Outline platelets.
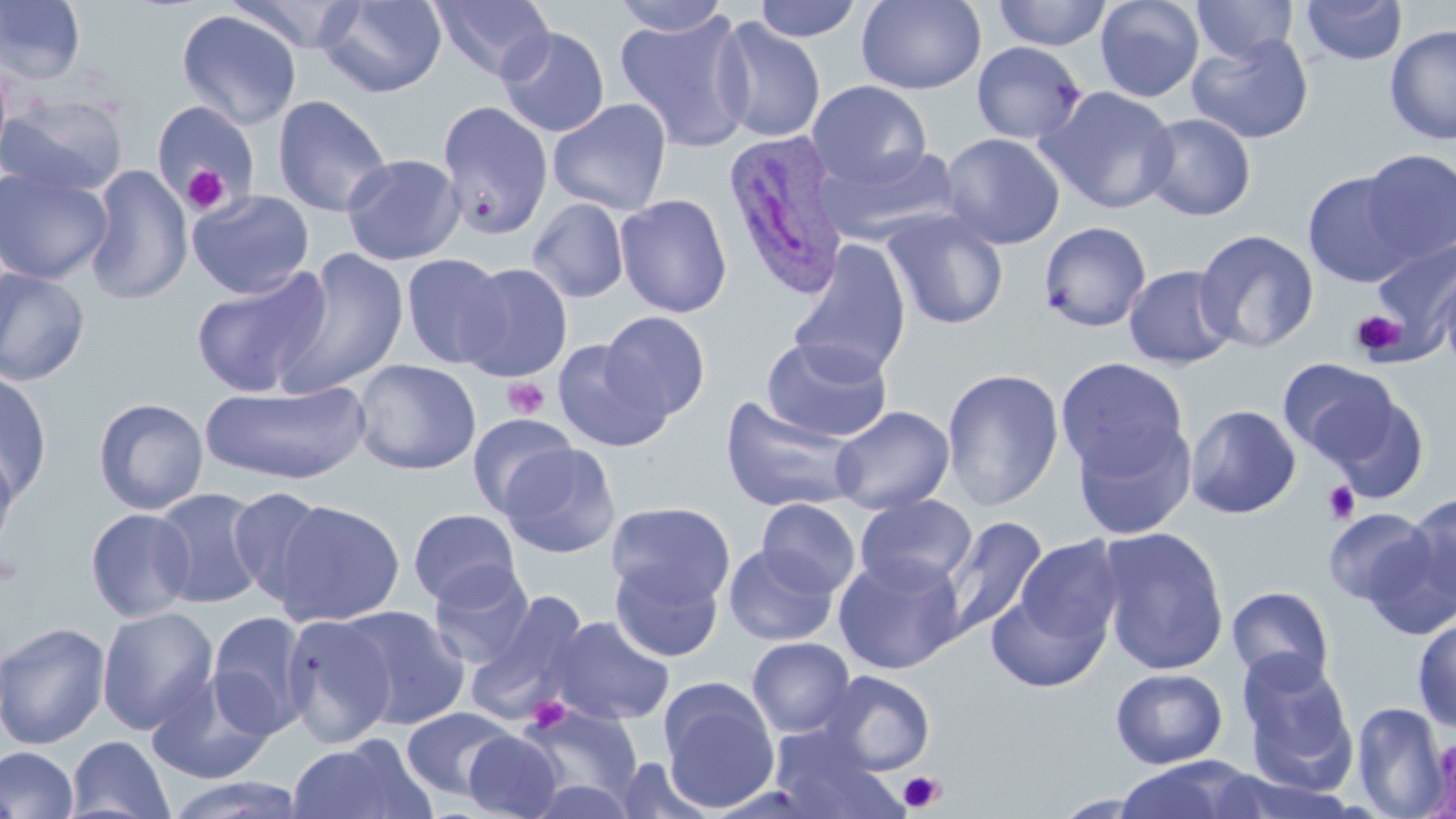
Approximate bounding boxes as named x1/y1/x2/y2 corners in pixels.
Platelets: (x1=182, y1=165, x2=229, y2=214), (x1=1351, y1=311, x2=1405, y2=359), (x1=503, y1=377, x2=549, y2=420), (x1=1323, y1=480, x2=1361, y2=524), (x1=524, y1=696, x2=572, y2=733), (x1=897, y1=770, x2=945, y2=813).

Uninfected red blood cell locations: (x1=0, y1=0, x2=86, y2=84), (x1=227, y1=0, x2=366, y2=54), (x1=316, y1=0, x2=447, y2=98), (x1=429, y1=0, x2=555, y2=82), (x1=609, y1=0, x2=734, y2=38), (x1=753, y1=0, x2=864, y2=42), (x1=856, y1=0, x2=986, y2=94), (x1=992, y1=0, x2=1112, y2=50), (x1=1094, y1=0, x2=1205, y2=103), (x1=1191, y1=0, x2=1298, y2=63), (x1=1300, y1=0, x2=1408, y2=66), (x1=175, y1=9, x2=302, y2=130), (x1=615, y1=9, x2=755, y2=152), (x1=712, y1=17, x2=826, y2=143), (x1=1384, y1=24, x2=1456, y2=144), (x1=497, y1=26, x2=610, y2=138), (x1=1186, y1=33, x2=1314, y2=145), (x1=971, y1=41, x2=1087, y2=145), (x1=0, y1=56, x2=13, y2=167), (x1=807, y1=79, x2=932, y2=188), (x1=1039, y1=86, x2=1178, y2=214), (x1=0, y1=95, x2=128, y2=197), (x1=272, y1=95, x2=392, y2=217), (x1=547, y1=98, x2=672, y2=215), (x1=150, y1=100, x2=260, y2=213), (x1=437, y1=100, x2=553, y2=240), (x1=1139, y1=113, x2=1256, y2=221), (x1=940, y1=132, x2=1065, y2=250), (x1=817, y1=143, x2=960, y2=245), (x1=1359, y1=150, x2=1456, y2=262), (x1=341, y1=153, x2=464, y2=266), (x1=85, y1=164, x2=192, y2=305), (x1=0, y1=166, x2=113, y2=285), (x1=1302, y1=169, x2=1419, y2=288), (x1=187, y1=190, x2=315, y2=298), (x1=615, y1=193, x2=732, y2=318), (x1=527, y1=199, x2=629, y2=303), (x1=881, y1=209, x2=1009, y2=330), (x1=1038, y1=221, x2=1152, y2=332), (x1=1194, y1=228, x2=1320, y2=353), (x1=1370, y1=236, x2=1456, y2=354), (x1=787, y1=240, x2=912, y2=380), (x1=271, y1=247, x2=410, y2=398), (x1=400, y1=252, x2=508, y2=369), (x1=458, y1=262, x2=573, y2=382), (x1=1123, y1=264, x2=1238, y2=370), (x1=0, y1=266, x2=91, y2=386), (x1=192, y1=266, x2=331, y2=399), (x1=1438, y1=268, x2=1456, y2=378), (x1=600, y1=311, x2=711, y2=419), (x1=761, y1=335, x2=892, y2=443), (x1=552, y1=339, x2=671, y2=452), (x1=1055, y1=357, x2=1190, y2=479), (x1=1278, y1=358, x2=1399, y2=465), (x1=352, y1=359, x2=482, y2=475), (x1=941, y1=367, x2=1065, y2=511), (x1=0, y1=369, x2=53, y2=501), (x1=200, y1=381, x2=370, y2=485), (x1=1323, y1=391, x2=1430, y2=503), (x1=720, y1=396, x2=864, y2=513), (x1=93, y1=397, x2=209, y2=515), (x1=1185, y1=404, x2=1301, y2=519), (x1=829, y1=405, x2=955, y2=514), (x1=467, y1=413, x2=579, y2=517), (x1=1072, y1=418, x2=1196, y2=540), (x1=0, y1=439, x2=20, y2=562), (x1=499, y1=442, x2=621, y2=559), (x1=151, y1=487, x2=268, y2=609), (x1=228, y1=487, x2=332, y2=605), (x1=1403, y1=492, x2=1456, y2=607), (x1=854, y1=494, x2=978, y2=594), (x1=269, y1=498, x2=406, y2=627), (x1=757, y1=498, x2=861, y2=597), (x1=606, y1=501, x2=736, y2=608), (x1=84, y1=507, x2=196, y2=622), (x1=1323, y1=507, x2=1433, y2=606), (x1=408, y1=508, x2=521, y2=607), (x1=938, y1=515, x2=1048, y2=639), (x1=1096, y1=526, x2=1231, y2=675), (x1=1361, y1=527, x2=1456, y2=641), (x1=1014, y1=536, x2=1124, y2=648), (x1=724, y1=543, x2=838, y2=646), (x1=833, y1=553, x2=965, y2=674), (x1=610, y1=560, x2=723, y2=662), (x1=427, y1=562, x2=536, y2=669), (x1=1227, y1=585, x2=1335, y2=687), (x1=987, y1=587, x2=1109, y2=693), (x1=465, y1=590, x2=591, y2=723), (x1=338, y1=605, x2=470, y2=729), (x1=97, y1=606, x2=219, y2=734), (x1=206, y1=611, x2=312, y2=738), (x1=281, y1=612, x2=397, y2=747), (x1=546, y1=616, x2=675, y2=726), (x1=1412, y1=616, x2=1456, y2=732), (x1=0, y1=621, x2=111, y2=750), (x1=746, y1=637, x2=856, y2=737), (x1=1237, y1=652, x2=1359, y2=788), (x1=1110, y1=667, x2=1228, y2=769), (x1=146, y1=670, x2=277, y2=784), (x1=819, y1=670, x2=936, y2=775), (x1=659, y1=680, x2=780, y2=812), (x1=1351, y1=701, x2=1449, y2=818), (x1=517, y1=704, x2=643, y2=808), (x1=401, y1=706, x2=518, y2=800), (x1=768, y1=725, x2=899, y2=817), (x1=462, y1=731, x2=564, y2=819), (x1=66, y1=735, x2=175, y2=819), (x1=286, y1=736, x2=433, y2=819), (x1=0, y1=746, x2=79, y2=819), (x1=613, y1=758, x2=716, y2=818), (x1=1112, y1=760, x2=1263, y2=817), (x1=162, y1=774, x2=309, y2=818), (x1=525, y1=778, x2=638, y2=818). Plasmodium ovale-infected red blood cell locations: (x1=721, y1=131, x2=850, y2=299). Slide-level diagnosis: Plasmodium ovale. 1000x magnification. May-Grünwald-Giemsa-stained preparation. Image is 1456×819 pixels. One field of a larger specimen. Light microscopy. Thin blood film.